Assess this cell for malaria.
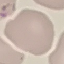

It is uninfected.

Summary:
  - Preparation: thin blood smear
  - Stain: Giemsa
  - Image type: automatically extracted cell patch, resized to 64 × 64 pixels
  - Capture: smartphone camera at the microscope eyepiece